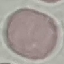
Result: no malaria parasites seen. Thin smear of blood. Cell patch, automatically extracted from a larger field of view and resized to 64 × 64 pixels. Photographed with a smartphone camera at the microscope eyepiece. Giemsa-stained preparation.